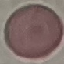

Summary:
  - Malaria status: uninfected
  - Preparation: thin blood film
  - Capture: smartphone camera at the microscope eyepiece
  - Image type: cell patch, automatically extracted from a larger field of view and resized to 64 × 64 pixels
  - Stain: Giemsa